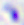

Summary:
  - Magnification: 400x
  - Modality: photomicrograph
  - Identification: Toxoplasma gondii